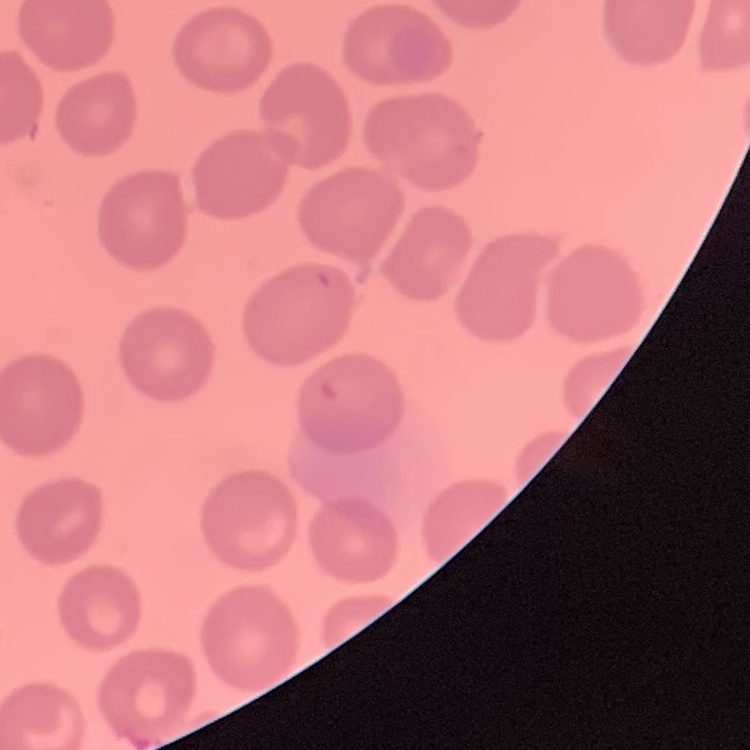

red blood cell morphology = no rouleaux formation
stain = Field's or Giemsa
preparation = thin blood smear
image type = square crop of a larger photomicrograph